Locate and identify every blood parasite.
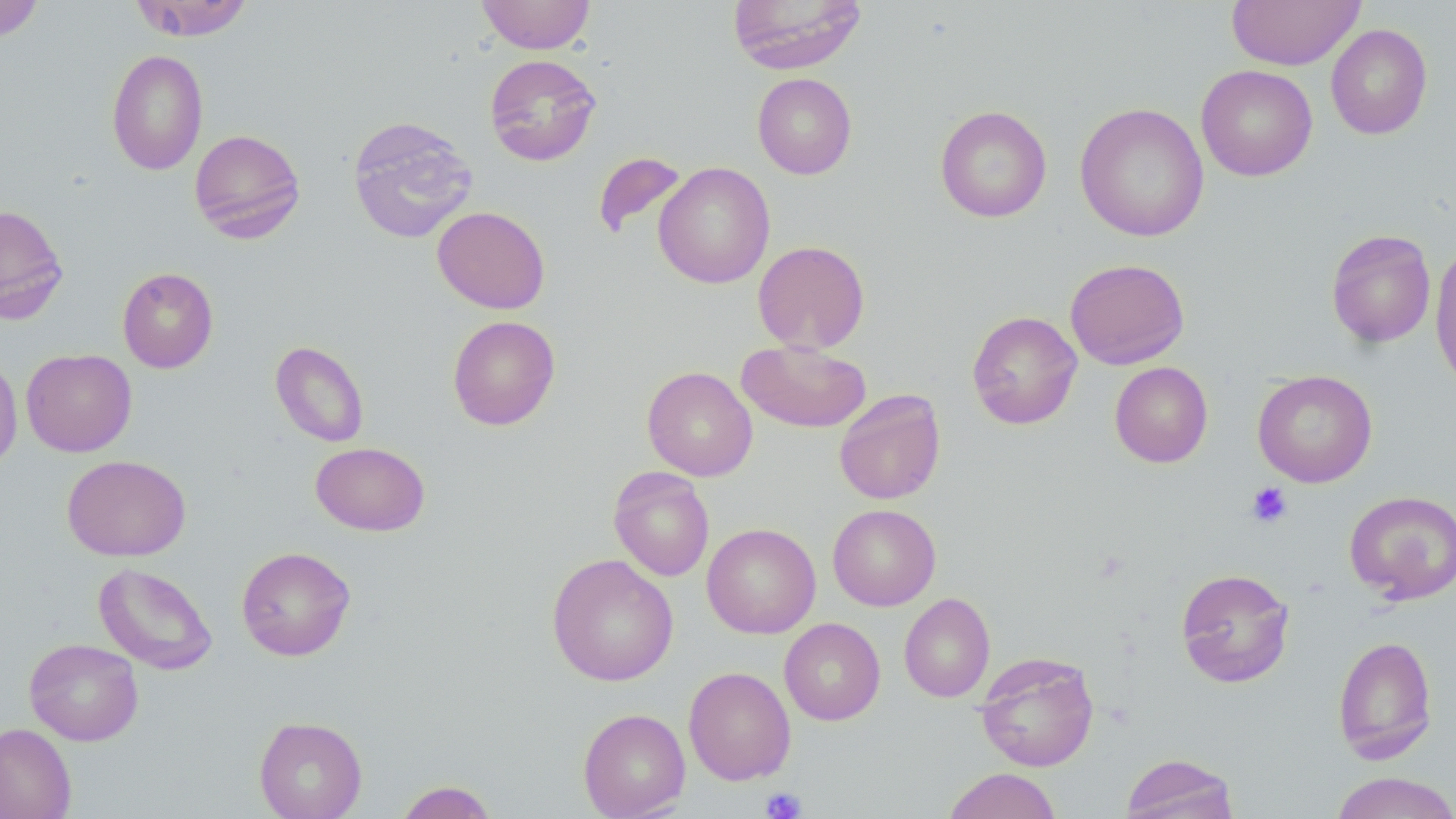

No blood parasites observed.

Summary:
  - Coordinate format: approximate bounding boxes as named x1/y1/x2/y2 corners in pixels
  - Platelet locations: (x1=1247, y1=482, x2=1292, y2=528), (x1=760, y1=786, x2=807, y2=818)
  - Uninfected red blood cell locations: (x1=130, y1=0, x2=254, y2=41), (x1=477, y1=0, x2=595, y2=54), (x1=726, y1=0, x2=867, y2=74), (x1=1226, y1=0, x2=1364, y2=70), (x1=0, y1=1, x2=44, y2=42), (x1=1326, y1=24, x2=1432, y2=140), (x1=106, y1=49, x2=208, y2=175), (x1=484, y1=54, x2=601, y2=166), (x1=1196, y1=64, x2=1317, y2=181), (x1=753, y1=73, x2=857, y2=179), (x1=1075, y1=102, x2=1210, y2=242), (x1=935, y1=105, x2=1052, y2=223), (x1=346, y1=115, x2=479, y2=244), (x1=189, y1=128, x2=306, y2=243), (x1=592, y1=151, x2=687, y2=240), (x1=654, y1=162, x2=775, y2=289), (x1=0, y1=203, x2=69, y2=324), (x1=432, y1=206, x2=550, y2=314), (x1=1326, y1=229, x2=1436, y2=348), (x1=753, y1=240, x2=870, y2=354), (x1=1430, y1=243, x2=1456, y2=391), (x1=1065, y1=258, x2=1190, y2=370), (x1=117, y1=267, x2=218, y2=373), (x1=967, y1=310, x2=1082, y2=430), (x1=447, y1=315, x2=560, y2=431), (x1=736, y1=339, x2=871, y2=433), (x1=271, y1=341, x2=369, y2=448), (x1=21, y1=348, x2=137, y2=457), (x1=0, y1=350, x2=23, y2=472), (x1=1109, y1=362, x2=1213, y2=468), (x1=642, y1=366, x2=757, y2=481), (x1=1252, y1=369, x2=1378, y2=487), (x1=834, y1=389, x2=946, y2=505), (x1=311, y1=442, x2=430, y2=536), (x1=62, y1=455, x2=191, y2=561), (x1=609, y1=467, x2=714, y2=581), (x1=1344, y1=490, x2=1456, y2=604), (x1=827, y1=504, x2=941, y2=611), (x1=702, y1=523, x2=820, y2=638), (x1=236, y1=546, x2=356, y2=661), (x1=547, y1=553, x2=679, y2=686), (x1=93, y1=562, x2=218, y2=675), (x1=1176, y1=568, x2=1295, y2=688), (x1=899, y1=593, x2=995, y2=702), (x1=779, y1=618, x2=885, y2=725), (x1=1332, y1=635, x2=1438, y2=764), (x1=24, y1=638, x2=143, y2=746), (x1=975, y1=652, x2=1099, y2=772), (x1=683, y1=666, x2=796, y2=784), (x1=578, y1=708, x2=690, y2=818), (x1=254, y1=716, x2=367, y2=819), (x1=0, y1=723, x2=76, y2=819), (x1=1120, y1=753, x2=1240, y2=819), (x1=943, y1=767, x2=1062, y2=819), (x1=1329, y1=771, x2=1456, y2=819), (x1=395, y1=780, x2=499, y2=819)
  - Slide-level diagnosis: no evidence of blood parasites
  - Stain: May-Grünwald-Giemsa
  - Field of view: one of a larger specimen
  - Modality: light microscopy
  - Preparation: thin blood smear
  - Magnification: 1000x
  - Image size: 1456×819 pixels